Look for parasitized red blood cells.
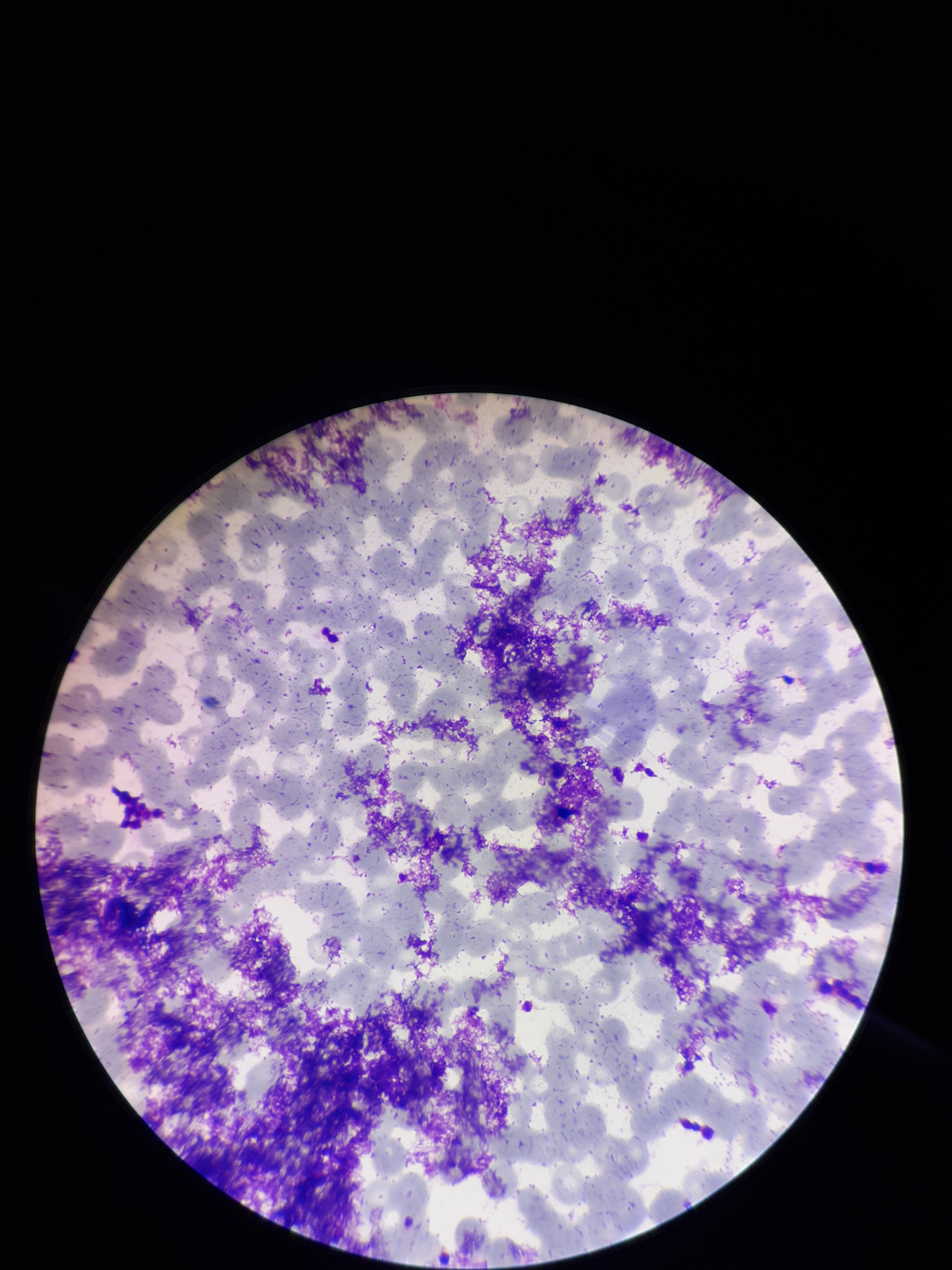
None detected.

Red blood cell count: 312. One field from this slide. Image is 952×1270 pixels. Parasitized red blood cell count: 0. Giemsa stain. Patient malaria status: negative. Photographed through the microscope eyepiece with a smartphone camera. Preparation: thin smear.